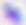

Toxoplasma gondii is seen. 400x magnification. Micrograph.